Name the blood parasite species.
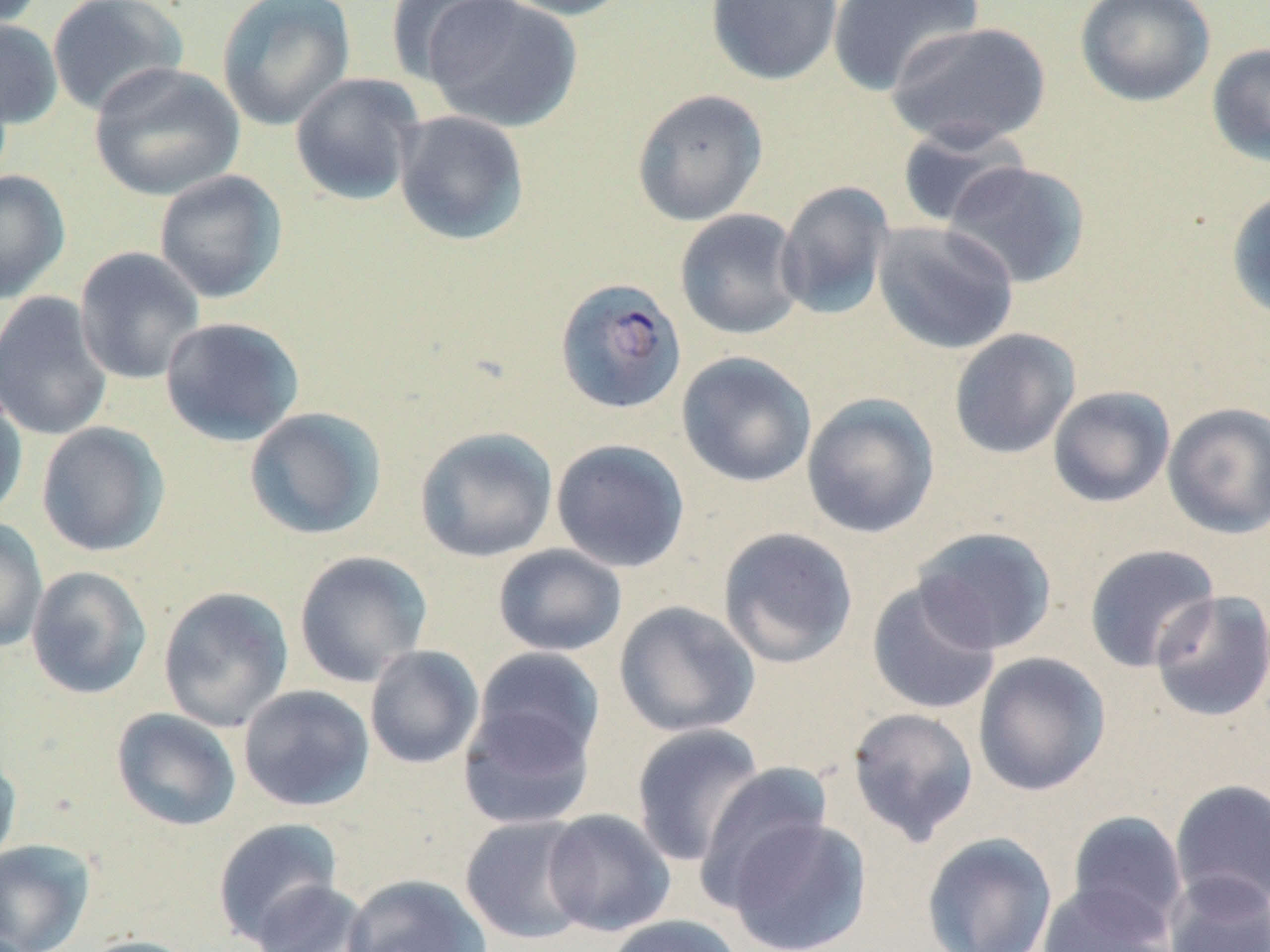

Plasmodium falciparum.

magnification = 1000x
field of view = single
stain = May-Grünwald-Giemsa
Plasmodium falciparum-infected red blood cell locations = approximate bounding boxes as (x1,y1)-(x2,y2) corner pairs in pixels: (555,277)-(687,415)
image size = 1270×952 pixels
uninfected red blood cell locations = approximate bounding boxes as (x1,y1)-(x2,y2) corner pairs in pixels: (46,0)-(189,117), (385,0)-(515,88), (419,0)-(583,132), (491,0)-(635,21), (706,0)-(843,86), (1075,0)-(1216,107), (217,1)-(356,130), (826,1)-(982,96), (0,17)-(63,130), (885,20)-(1052,150), (1207,43)-(1270,168), (89,62)-(244,201), (288,72)-(426,206), (631,88)-(769,226), (393,110)-(530,247), (895,123)-(1028,229), (943,161)-(1090,289), (0,170)-(71,303), (154,170)-(288,303), (775,180)-(896,321), (1226,187)-(1270,323), (674,208)-(806,341), (872,221)-(1019,355), (74,247)-(206,385), (0,292)-(114,442), (159,316)-(305,446), (948,328)-(1081,460), (676,351)-(817,488), (0,383)-(28,523), (1047,386)-(1175,508), (801,393)-(940,539), (1162,402)-(1270,539), (243,407)-(387,540), (36,421)-(170,557), (414,426)-(558,563), (551,438)-(691,573), (0,518)-(48,652), (912,526)-(1057,655), (717,527)-(859,668), (1083,543)-(1220,673), (493,544)-(627,657), (293,550)-(433,687), (26,565)-(152,700), (866,579)-(1001,715), (157,586)-(294,732), (1150,590)-(1270,723), (614,600)-(761,738), (364,645)-(484,770), (470,648)-(606,770), (972,652)-(1111,796), (238,684)-(375,812), (458,699)-(598,830), (846,706)-(980,845), (111,707)-(242,832), (630,723)-(766,867), (0,747)-(21,869), (695,763)-(833,905), (1169,779)-(1270,913), (541,809)-(676,937), (1067,811)-(1189,936), (459,814)-(596,945), (724,816)-(872,952), (212,817)-(345,945), (921,832)-(1057,952), (0,839)-(95,952), (1164,872)-(1269,952), (342,874)-(492,952), (250,880)-(373,952), (1037,883)-(1177,952), (604,914)-(743,952), (78,934)-(204,952)
modality = optical microscopy
preparation = thin blood film